Identify the parasite.
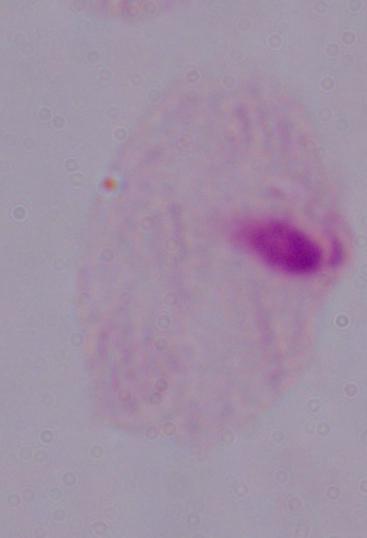

A trichomonad.

{
  "modality": "micrograph",
  "magnification": "1000x"
}